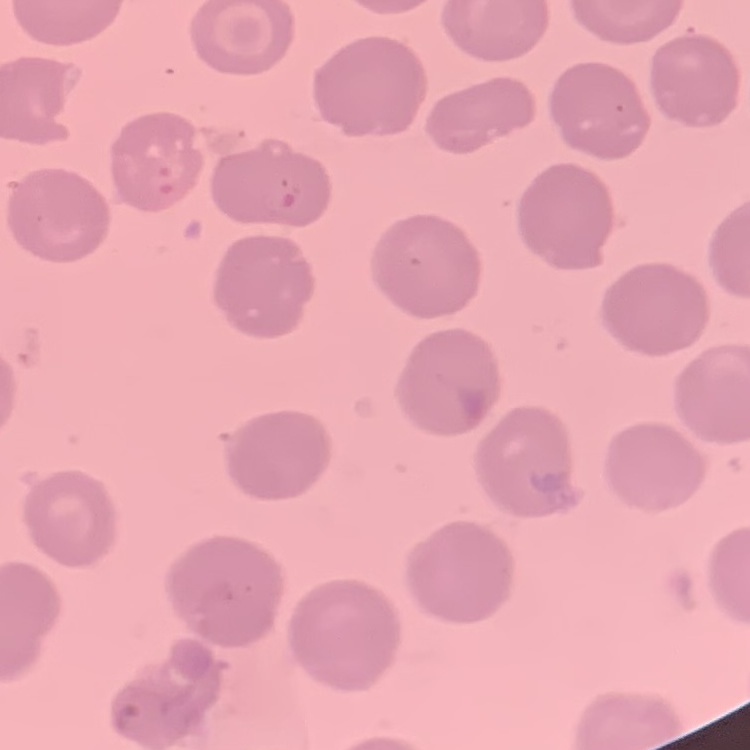 The erythrocytes show no rouleaux formation. Square crop of a larger photomicrograph. Thin blood smear. Field's or Giemsa stain.